Comment on the morphology of the erythrocytes.
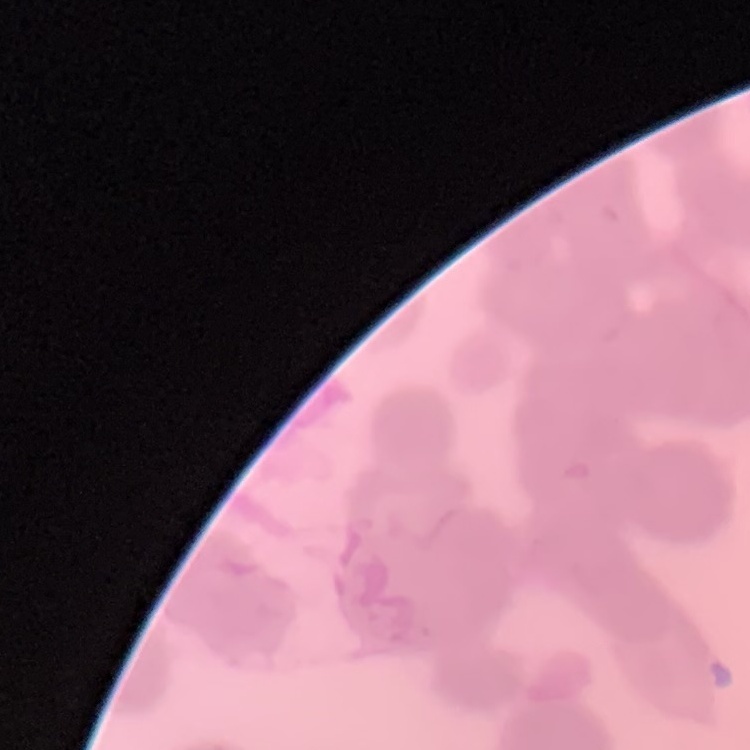
Rouleaux formation.

Summary:
  - Preparation: thin peripheral smear
  - Image type: one tile cut from a larger photomicrograph
  - Stain: Field's or Giemsa